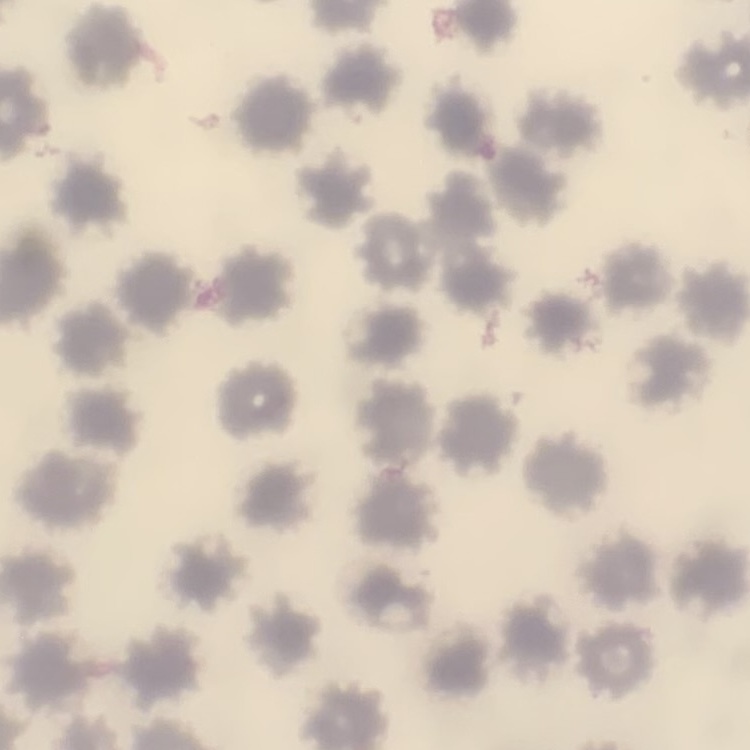
Summary:
  - Red blood cell morphology: no rouleaux formation
  - Stain: Field's or Giemsa
  - Image type: square crop of a larger photomicrograph
  - Preparation: thin blood film